Assess the morphology of the erythrocytes.
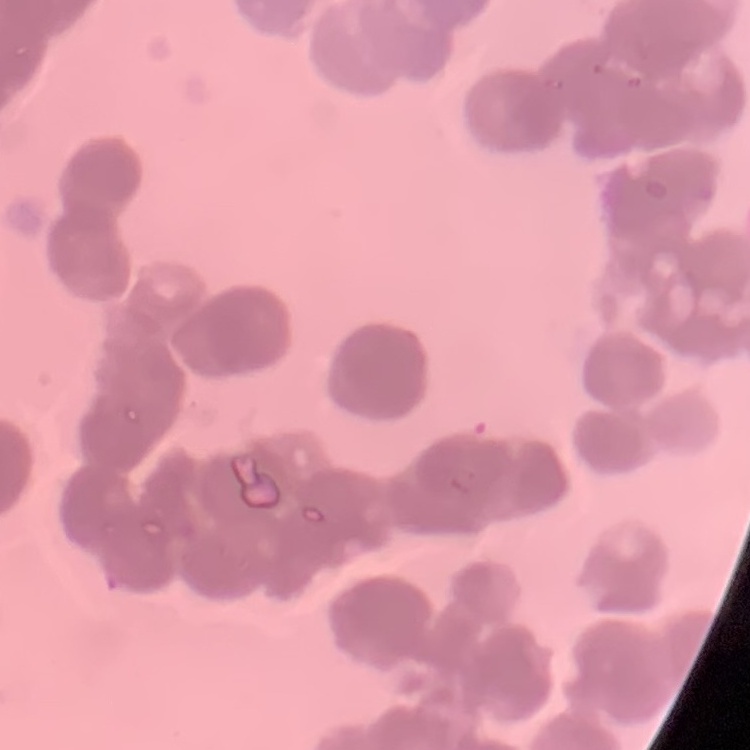
They show rouleaux formation.

Summary:
  - Image type: one tile cut from a larger photomicrograph
  - Preparation: thin blood film
  - Stain: Field's or Giemsa